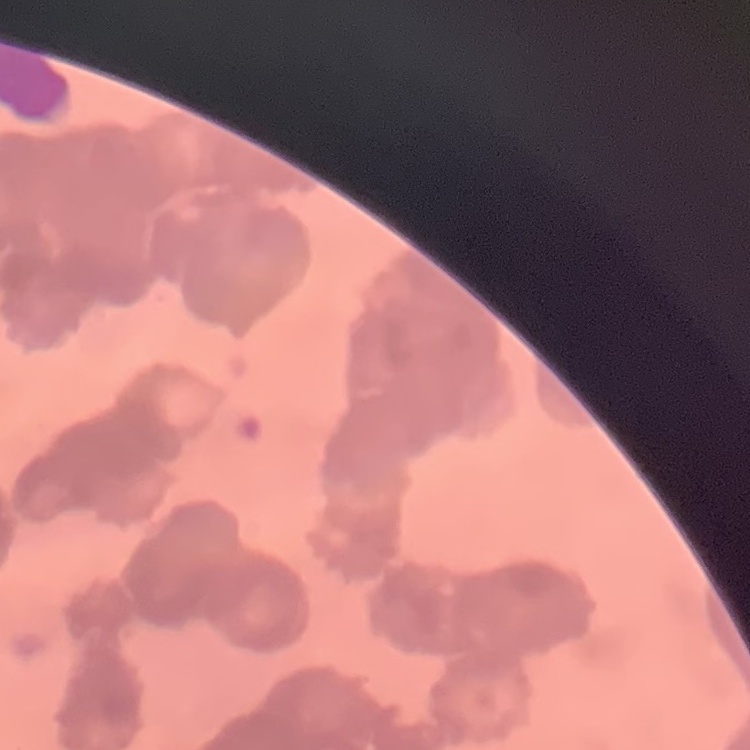 The erythrocytes show rouleaux formation. Square crop of a larger photomicrograph. Thin blood smear. Field's or Giemsa stain.